Locate and identify every blood parasite.
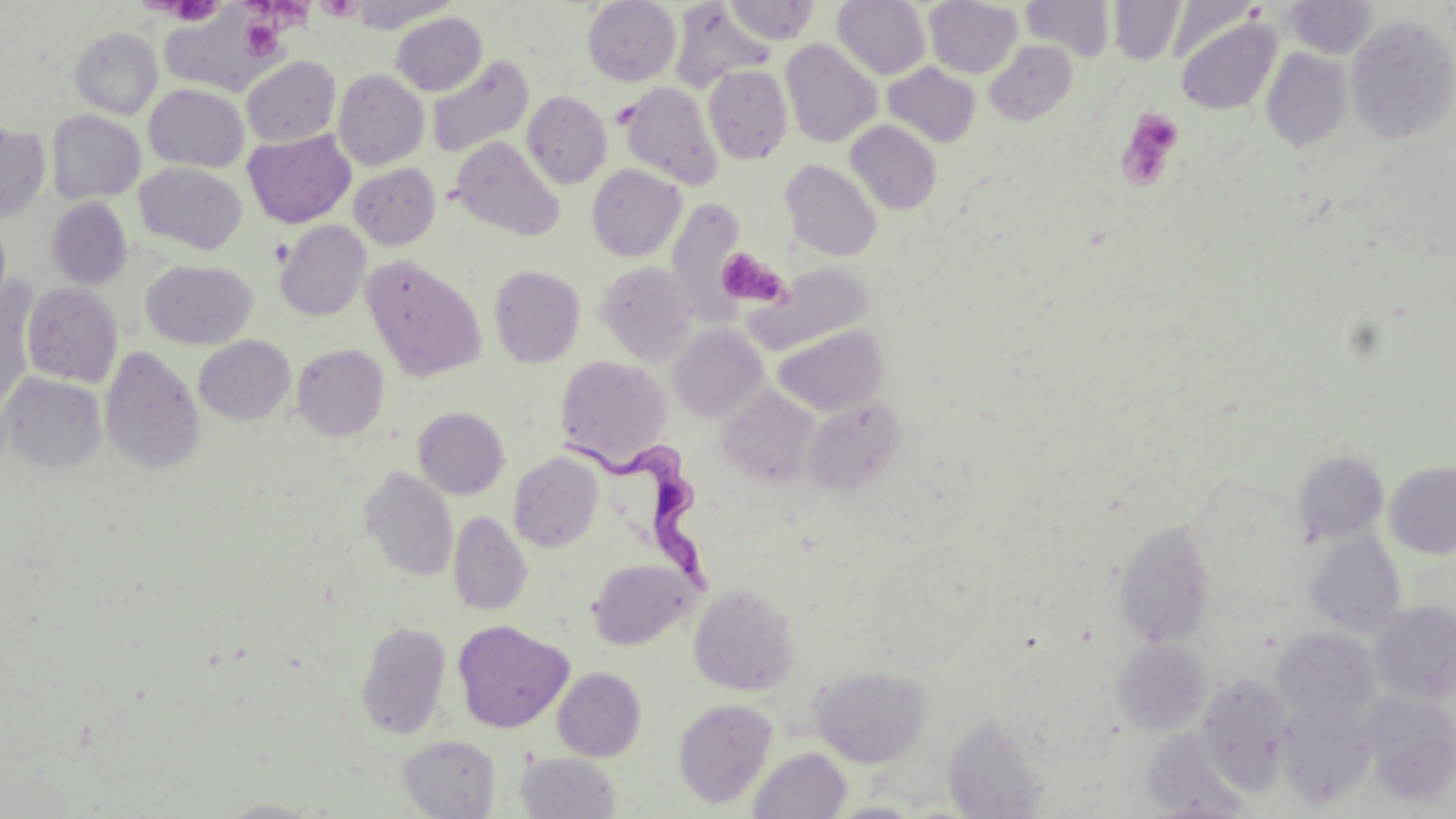

Approximate bounding boxes as (x1,y1)-(x2,y2) corner pairs in pixels.
Trypanosoma brucei: (563,435)-(717,601).
No Plasmodium falciparum, Plasmodium ovale, Plasmodium malariae, Plasmodium vivax, or Babesia divergens observed.

Summary:
  - Uninfected red blood cell locations: (350,0)-(458,32), (583,0)-(681,86), (724,0)-(819,44), (832,0)-(930,80), (924,0)-(1022,78), (1021,0)-(1116,60), (1285,0)-(1379,59), (1108,1)-(1185,64), (669,3)-(775,92), (162,10)-(288,88), (391,12)-(487,96), (1174,15)-(1281,115), (1345,15)-(1456,143), (70,27)-(163,119), (780,39)-(882,147), (984,40)-(1078,125), (1261,48)-(1353,151), (427,55)-(533,158), (241,56)-(341,147), (883,62)-(981,147), (703,65)-(793,164), (333,70)-(430,170), (144,83)-(249,172), (619,83)-(723,190), (522,92)-(612,188), (47,110)-(145,205), (846,120)-(942,215), (0,124)-(51,223), (243,130)-(355,228), (451,136)-(564,242), (780,159)-(881,262), (135,163)-(248,254), (349,163)-(440,250), (586,165)-(686,262), (47,197)-(132,289), (664,198)-(746,324), (0,220)-(10,312), (275,220)-(371,322), (361,256)-(487,382), (141,260)-(257,350), (596,262)-(697,366), (749,263)-(875,354), (489,265)-(586,368), (0,282)-(37,409), (21,282)-(122,387), (667,324)-(768,424), (773,325)-(888,417), (194,335)-(295,425), (293,344)-(389,441), (99,346)-(205,474), (554,355)-(673,470), (1,372)-(107,474), (719,387)-(820,488), (803,396)-(906,496), (414,407)-(509,499), (1292,449)-(1389,546), (509,452)-(604,552), (1385,460)-(1456,558), (360,467)-(458,582), (448,511)-(531,616), (1114,520)-(1217,648), (1304,528)-(1407,638), (587,557)-(699,650), (689,583)-(800,696), (1370,600)-(1456,704), (355,619)-(452,740), (453,620)-(573,733), (1271,626)-(1381,726), (1112,638)-(1212,735), (810,666)-(932,768), (553,667)-(646,761), (1197,674)-(1294,793), (1356,692)-(1456,807), (673,698)-(778,809), (1277,699)-(1380,811), (943,713)-(1049,818), (1142,728)-(1253,817), (399,734)-(501,818), (748,747)-(852,819), (514,752)-(622,819), (219,799)-(326,818), (824,801)-(928,818)
  - Platelet locations: (143,0)-(222,26), (237,0)-(316,30), (317,0)-(365,21), (241,17)-(286,60), (1115,107)-(1185,191), (716,248)-(790,309)
  - Slide-level diagnosis: Trypanosoma brucei
  - Field of view: one of a larger specimen
  - Image size: 1456×819 pixels
  - Modality: optical microscopy
  - Preparation: thin blood film
  - Magnification: 1000x
  - Stain: May-Grünwald-Giemsa